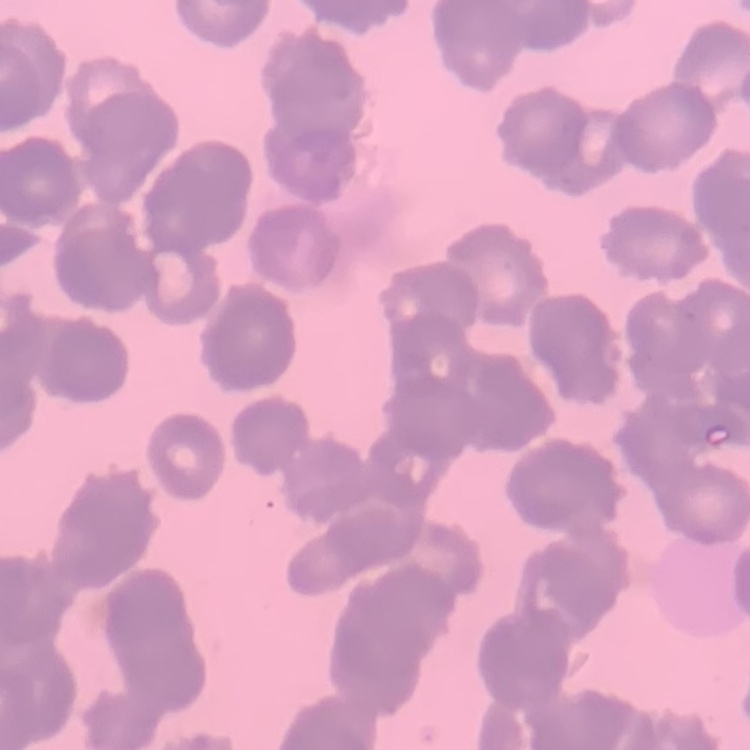
{
  "erythrocyte_morphology": "rouleaux formation",
  "image_type": "square crop of a larger photomicrograph",
  "preparation": "thin peripheral smear",
  "stain": "Field's or Giemsa"
}